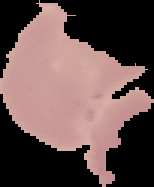
Image is 154×187 pixels. From a thin blood film. Malaria status: uninfected. Segmented cell region on a black background.